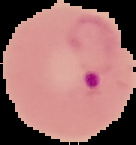
Cell region segmented out of the field of view; the surrounding area is masked to black. From a thin blood film. Image is 136×145 pixels. Result: malaria parasites identified.